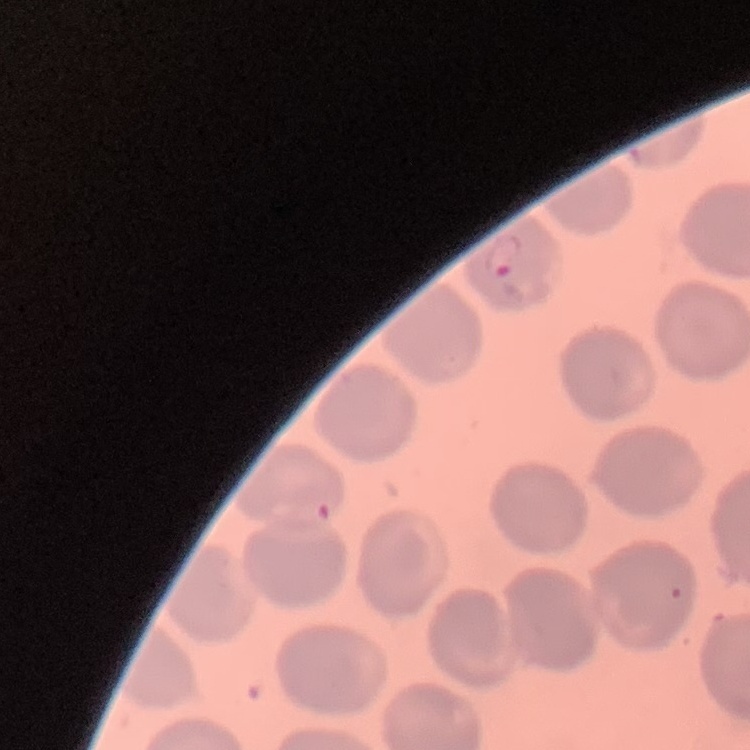

The erythrocytes show no rouleaux formation. Thin blood film. Stained with either Field's or Giemsa. One tile cut from a larger photomicrograph.